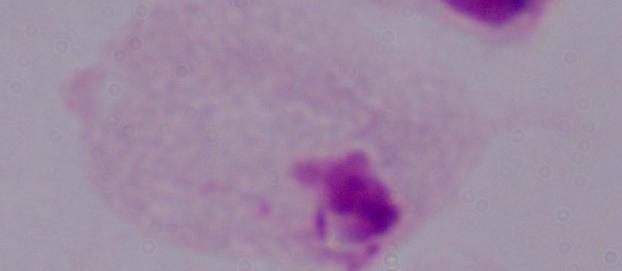

magnification: 1000x
modality: photomicrograph
identification: trichomonad